Describe the morphology of the red blood cells.
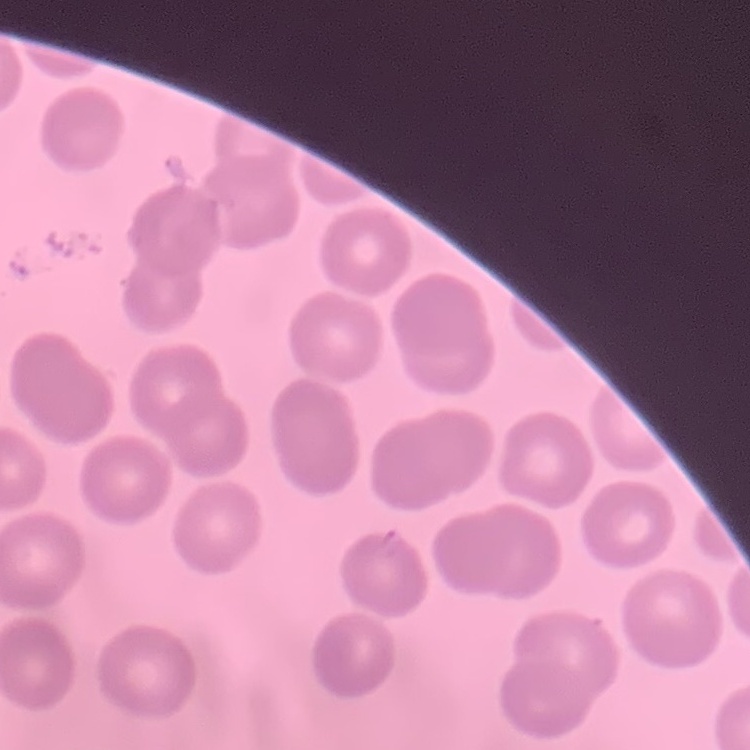

No rouleaux formation.

Thin blood smear. Stained with either Field's or Giemsa. Square crop of a larger photomicrograph.